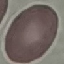 Malaria status: uninfected. Photographed with a smartphone camera at the microscope eyepiece. Thin blood smear. Cell patch, automatically extracted from a larger field of view and resized to 64 × 64 pixels. Giemsa-stained preparation.